Assess the morphology of the erythrocytes.
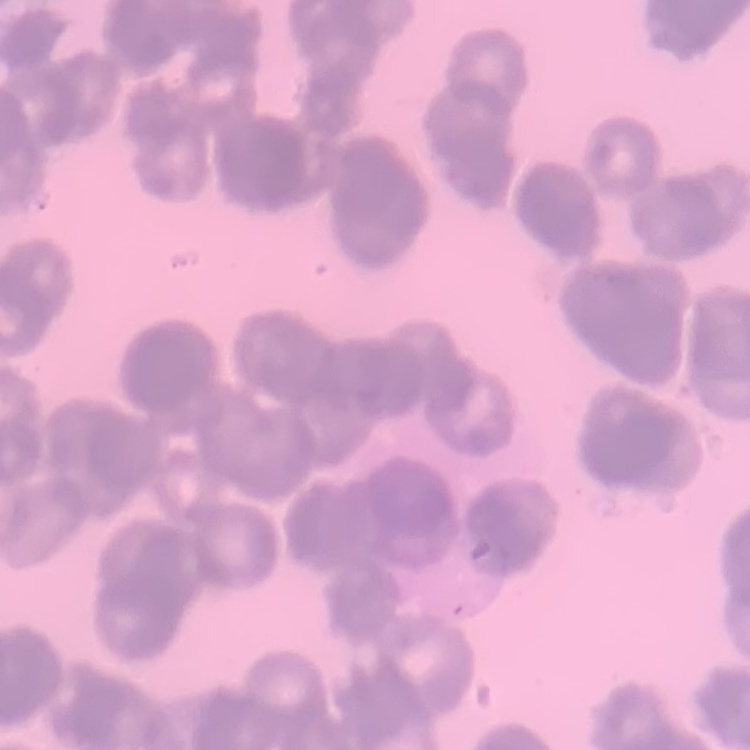

They show rouleaux formation.

preparation = thin blood film
image type = square crop of a larger photomicrograph
stain = Field's or Giemsa